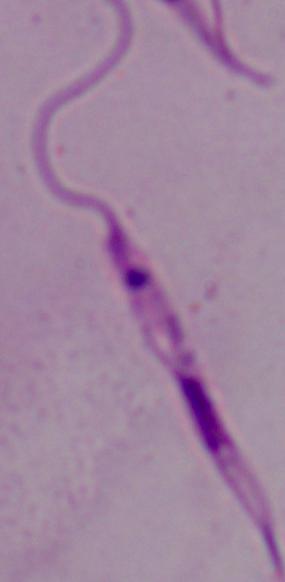

A Leishmania parasite is shown. Micrograph. Captured at 1000x magnification.